Locate every Plasmodium parasite by life-cycle stage, and every leukocyte.
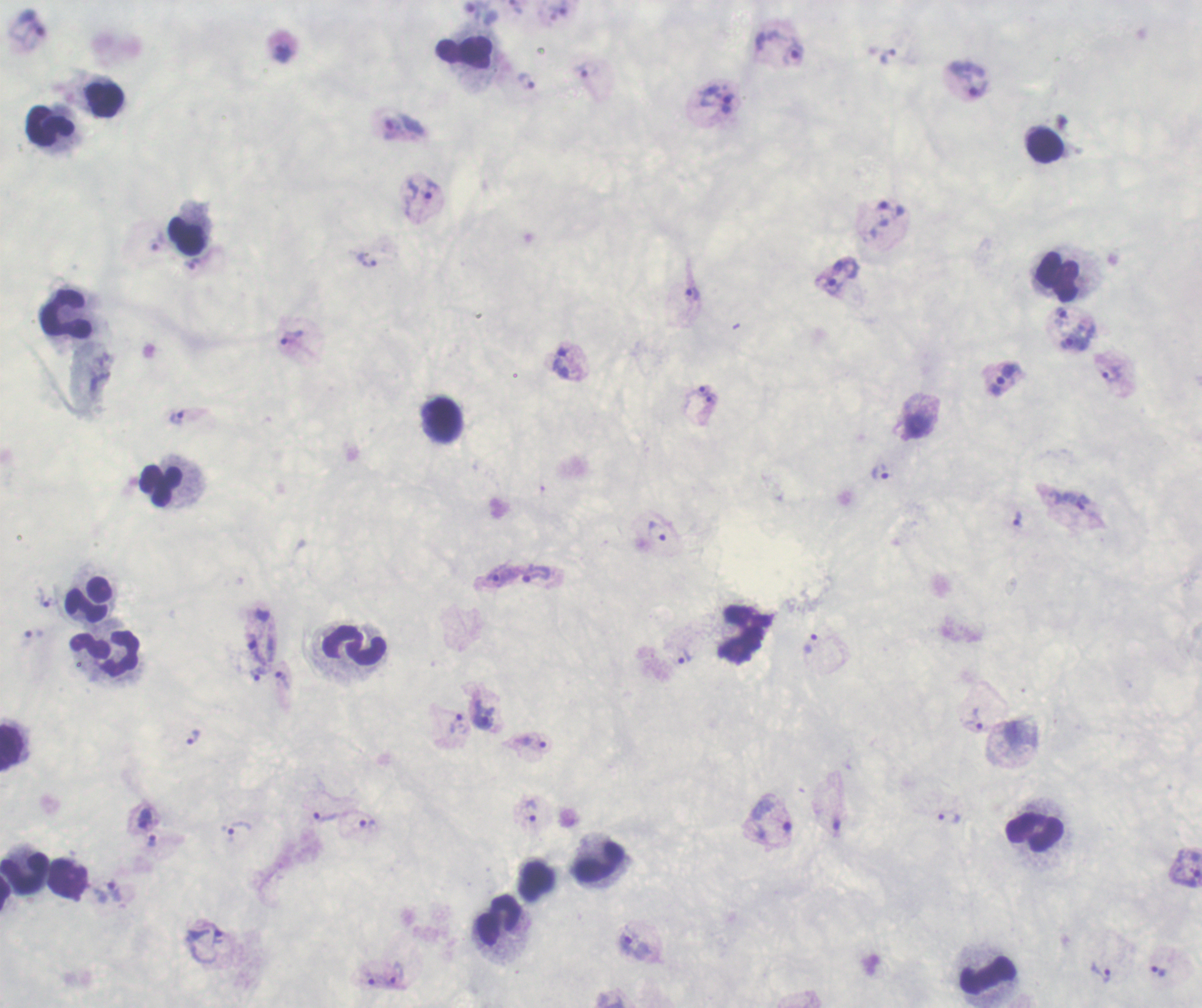
Approximate centers as [x, y] in pixels.
Trophozoites: [559, 9], [792, 53], [281, 54], [585, 71], [968, 78], [526, 80], [715, 99], [390, 125], [422, 191], [366, 259], [840, 276], [692, 294], [1075, 337], [291, 338], [1113, 374], [1003, 379], [176, 417], [879, 472], [1072, 500], [1018, 519], [658, 531], [500, 574], [537, 574], [45, 598], [812, 643], [259, 644], [684, 657], [261, 672], [283, 681], [484, 714], [974, 719], [458, 723], [193, 737], [535, 743], [531, 810], [324, 815], [948, 816], [145, 818], [772, 820], [366, 822], [835, 823], [236, 830], [152, 841], [1185, 867], [109, 893], [634, 943], [1158, 969], [1102, 971], [397, 973].
No schizont or gametocyte forms observed.
Leukocytes: [465, 53], [103, 97], [52, 126], [1044, 145], [187, 236], [1057, 278], [66, 314], [442, 419], [163, 486], [89, 601], [354, 646], [105, 652], [13, 748], [1036, 831], [599, 861], [24, 872], [68, 880], [499, 920], [988, 974].

Summary:
  - Field of view: one from this slide
  - Preparation: thick blood smear
  - Stain: Romanowsky
  - Background quality: poor
  - Image size: 1202×1008 pixels
  - Magnification: 100x
  - Context: previously used in a real diagnosis